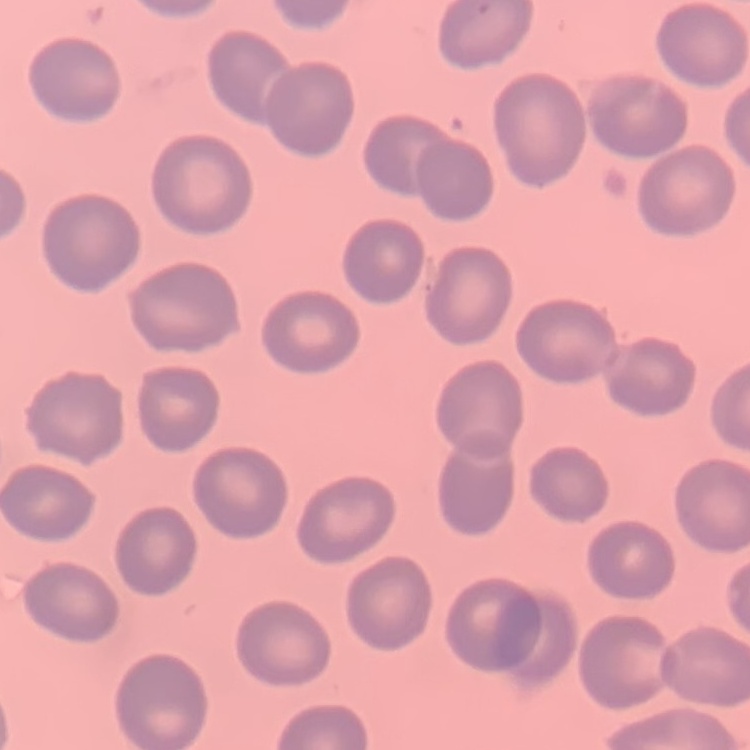
Summary:
  - Red blood cell morphology: no rouleaux formation
  - Preparation: thin blood smear
  - Stain: Field's or Giemsa
  - Image type: one tile cut from a larger photomicrograph